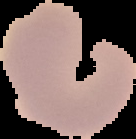
preparation = thin blood film
image size = 136×139 pixels
malaria status = uninfected
image type = segmented cell region on a black background